Identify the parasite.
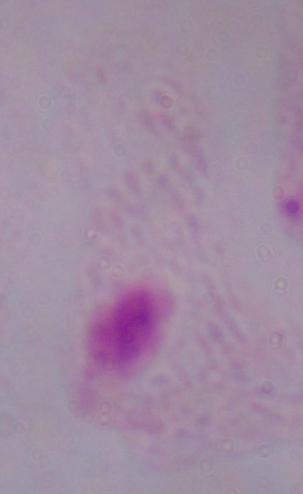

This is a trichomonad.

magnification: 1000x
modality: photomicrograph